Describe the morphology of the erythrocytes.
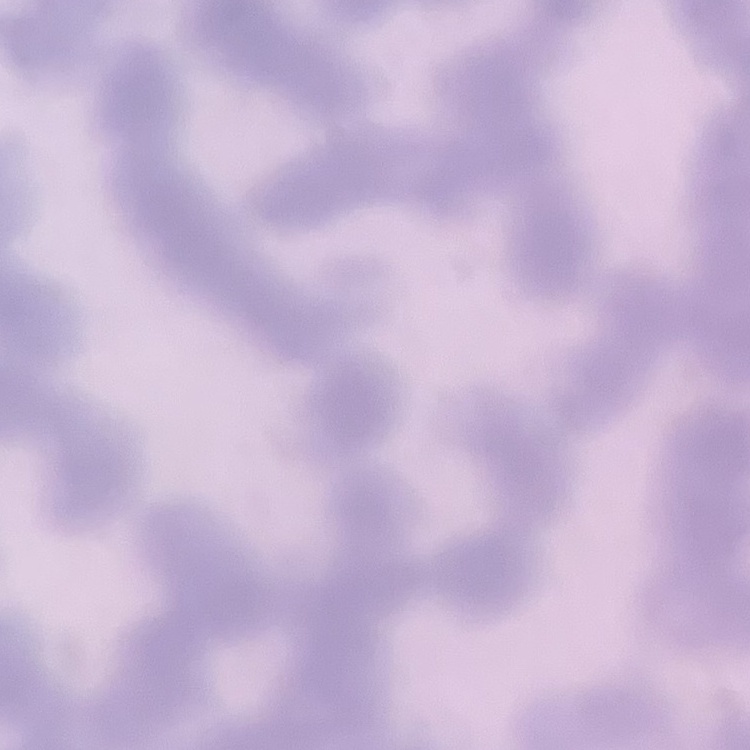
They show rouleaux formation.

Summary:
  - Stain: Field's or Giemsa
  - Preparation: thin peripheral smear
  - Image type: square crop of a larger photomicrograph